Point out malaria parasites and leukocytes.
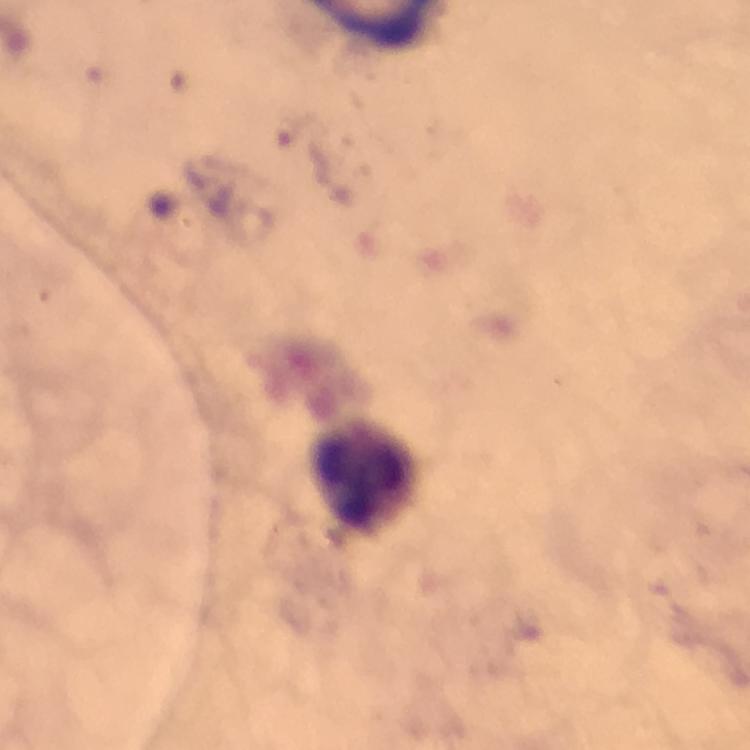

No malaria parasites detected.
Approximate centers as {x, y} in pixels.
Leukocytes: {366, 476}.

image size = 750×750 pixels
preparation = thick blood film
stain = Giemsa
context = from a malaria diagnostic workup
immersion oil = applied
magnification = 100x
capture = smartphone camera through the microscope
cropped from = a single field of view